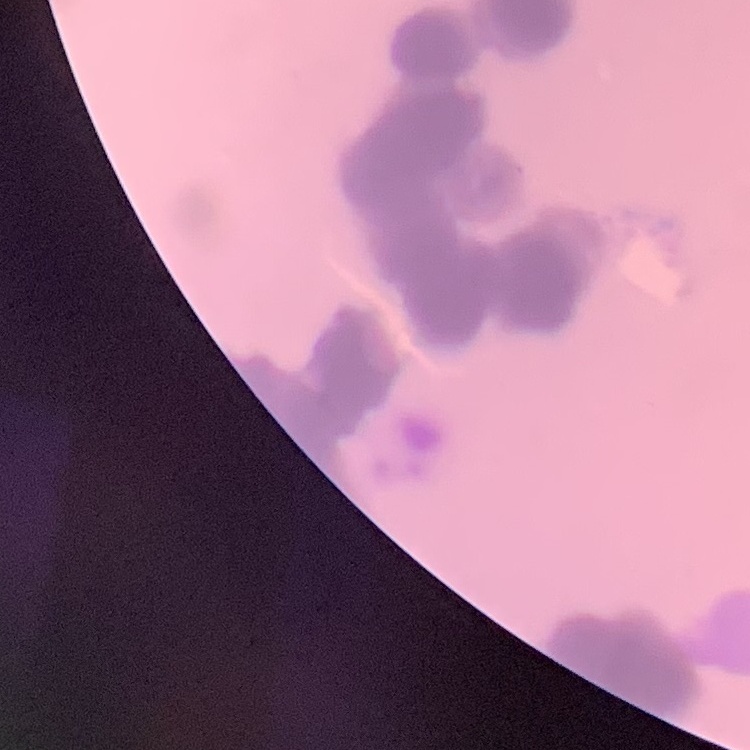

{
  "red_blood_cell_morphology": "rouleaux formation",
  "image_type": "square crop of a larger photomicrograph",
  "preparation": "thin peripheral smear",
  "stain": "Field's or Giemsa"
}